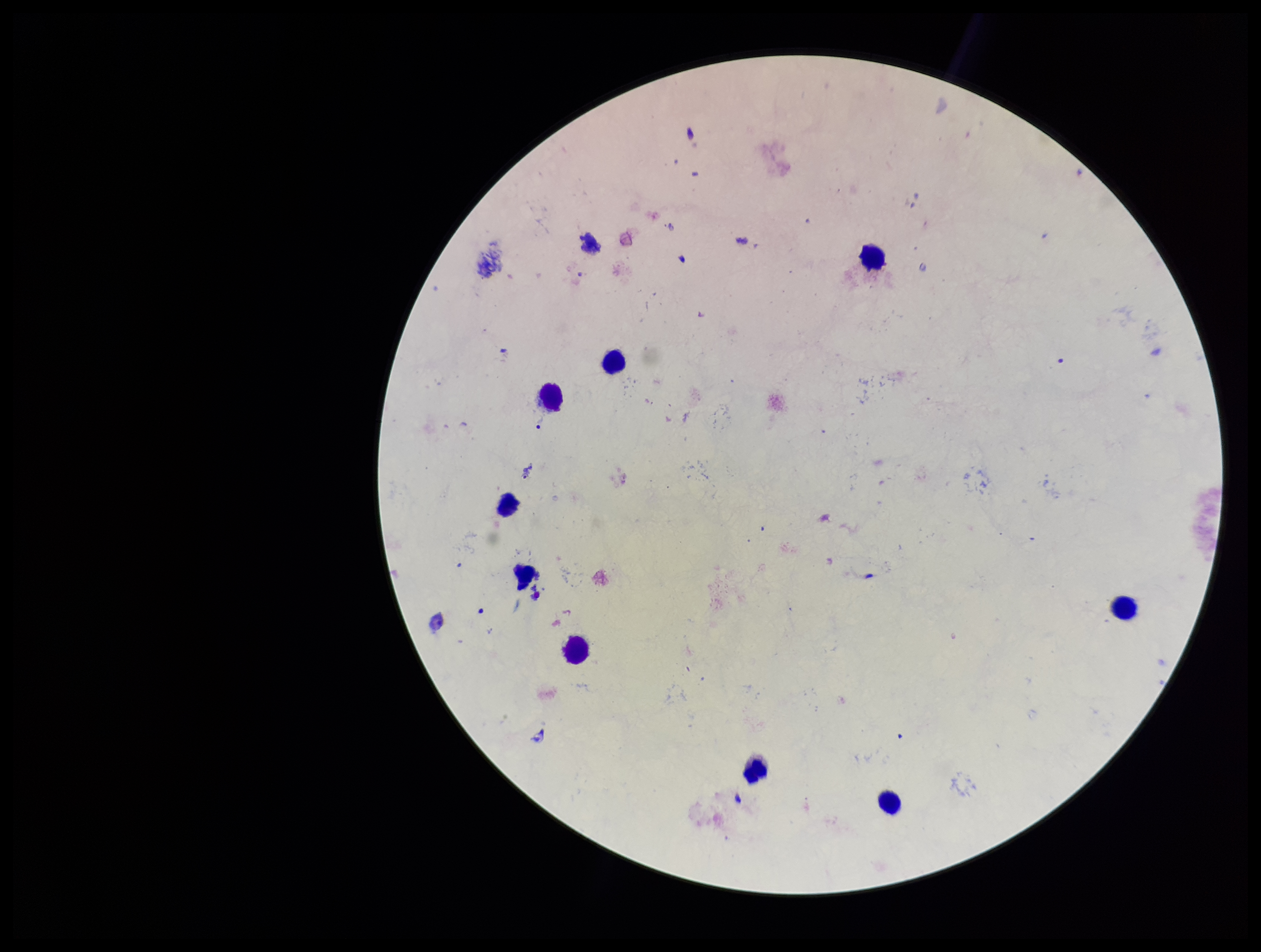

Summary:
  - Field of view: single
  - Image size: 1261×952 pixels
  - Parasite count: 0
  - Preparation: thick
  - Stain: Giemsa
  - Plasmodium parasites: none detected
  - Leukocyte count: 9
  - Patient malaria status: negative
  - Capture: smartphone photograph through the microscope eyepiece